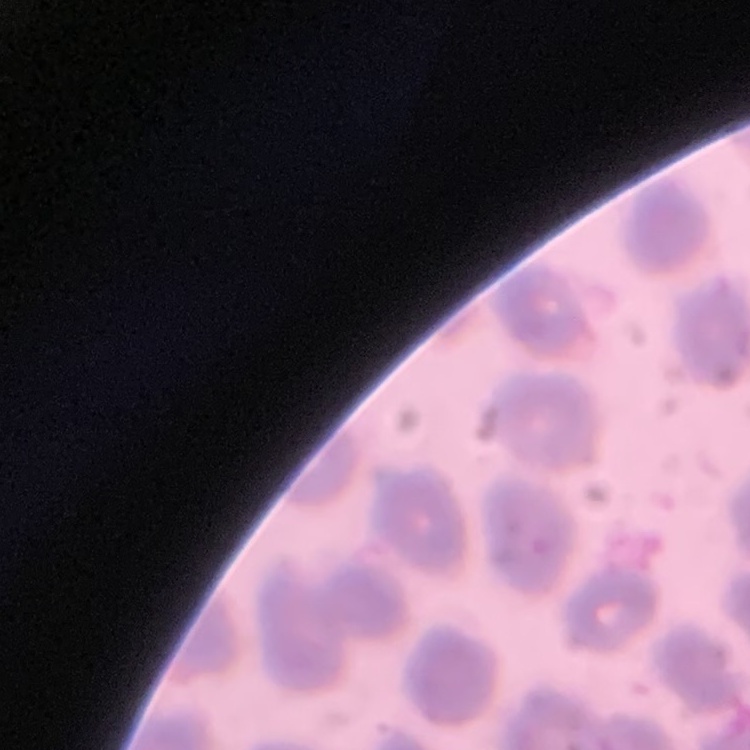
The red blood cells show no rouleaux formation. Thin blood film. Stained with either Field's or Giemsa. Square crop of a larger photomicrograph.